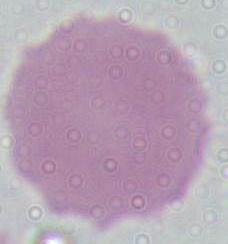

A red blood cell is shown. Photomicrograph. 1000x magnification.